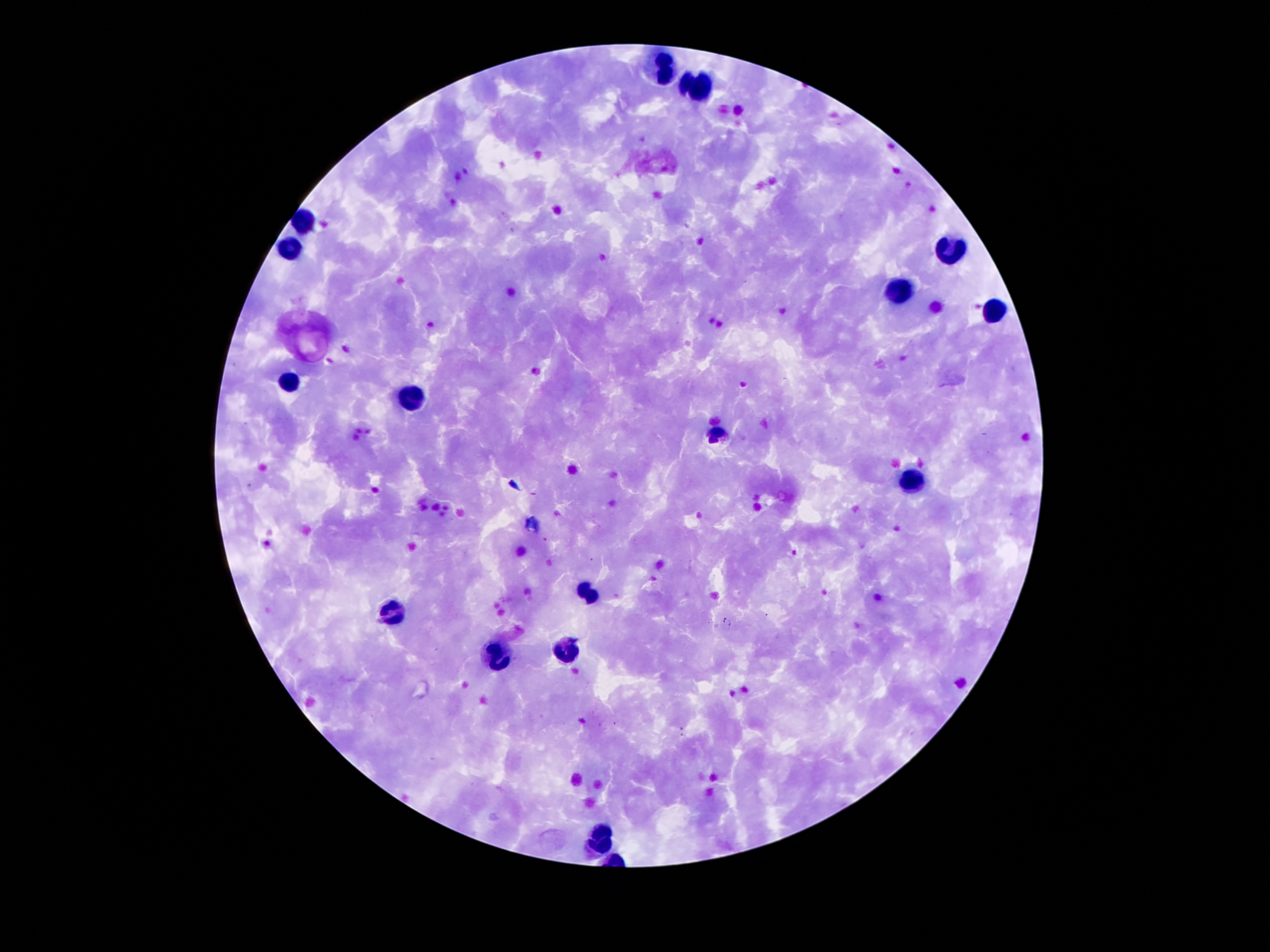
coordinate format = approximate centers as [x, y] in pixels
leukocyte locations = [664, 72], [705, 84], [302, 224], [952, 245], [288, 249], [898, 287], [997, 310], [292, 383], [407, 398], [718, 433], [913, 480], [593, 598], [394, 610], [568, 652], [495, 654], [602, 831]
Plasmodium parasite locations = [558, 511], [544, 539], [592, 560], [723, 619], [731, 624], [615, 724]
field of view = one from this slide
magnification = 100x
capture = smartphone camera through the microscope eyepiece
patient malaria status = positive for Plasmodium falciparum
image size = 1270×952 pixels
preparation = thick peripheral-blood smear
stain = Giemsa